Assess this cell for malaria.
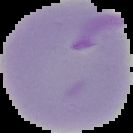
It is parasitized.

Summary:
  - Preparation: thin blood film
  - Image type: segmented cell region with the area outside set to black
  - Image size: 133×133 pixels